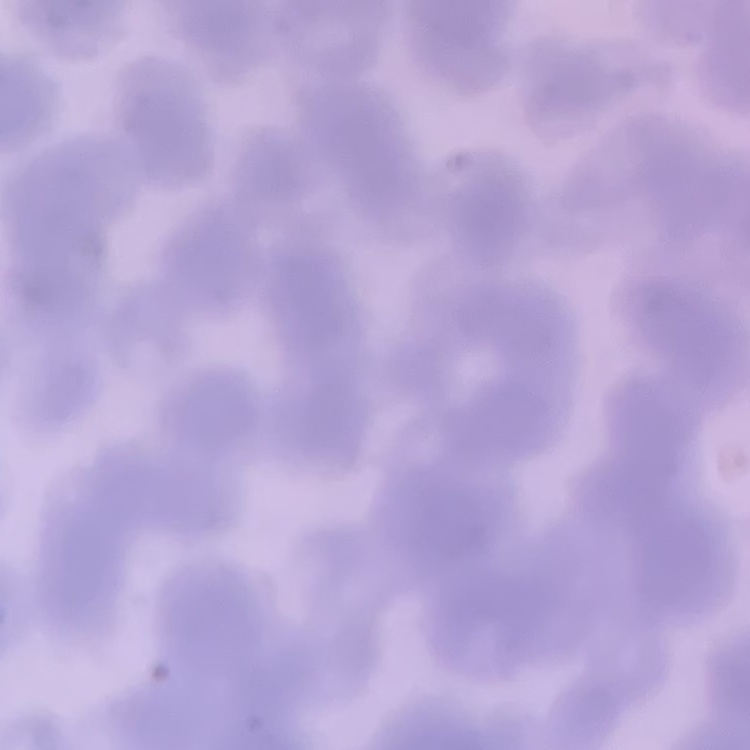

The red blood cells exhibit rouleaux formation. Thin blood film. One tile cut from a larger photomicrograph. Field's or Giemsa stain.